Classify this cell by malaria status.
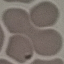
Parasitized.

{
  "capture": "smartphone through the microscope eyepiece",
  "stain": "Giemsa",
  "preparation": "thin smear",
  "image_type": "automatically extracted cell patch, resized to 64 × 64 pixels"
}